Locate every blood parasite and identify its species.
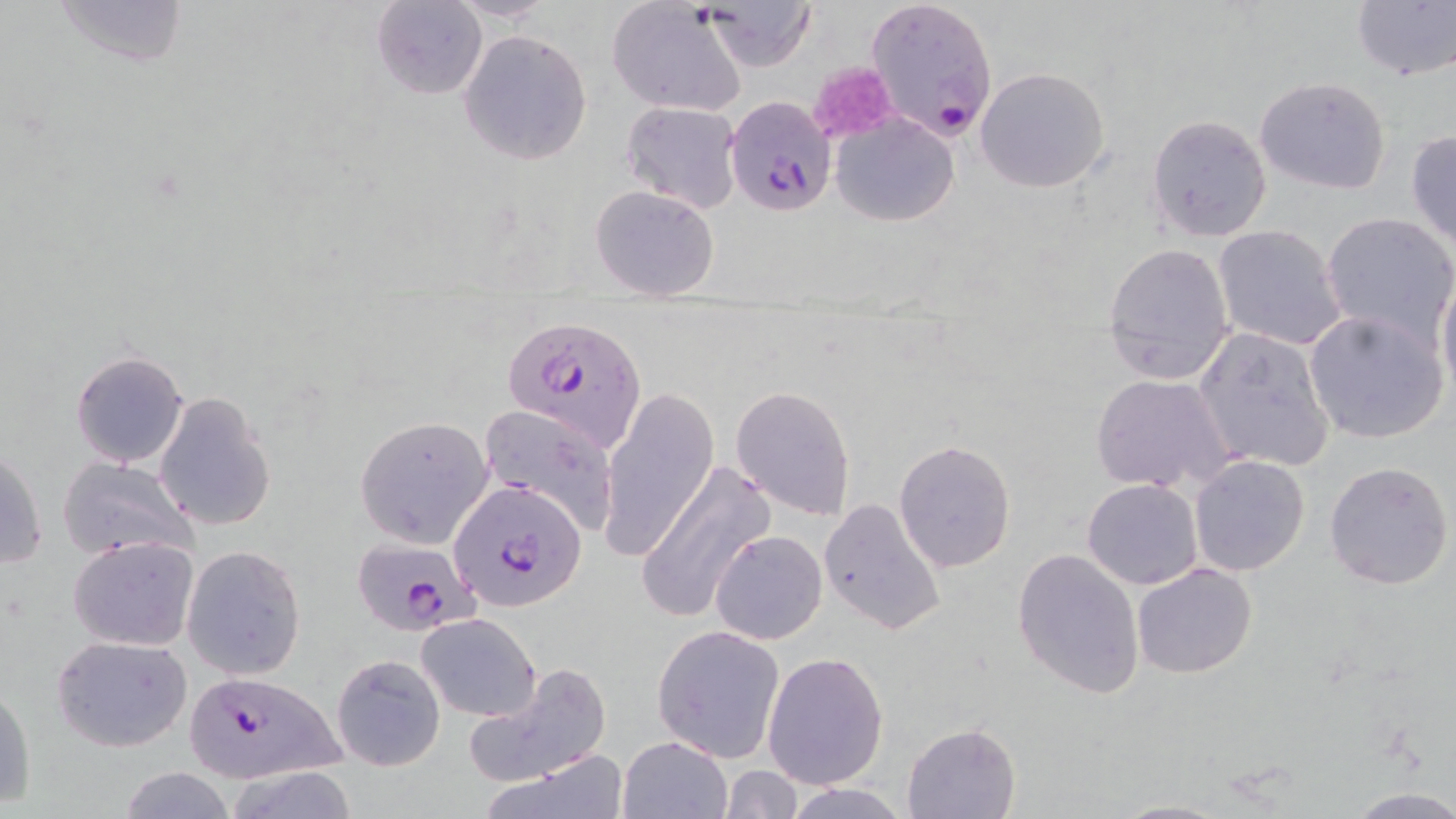
Approximate bounding boxes as (x1, y1, x2, y2) in pixels.
Plasmodium falciparum-infected red blood cells: (868, 0, 999, 141), (722, 94, 833, 216), (503, 313, 648, 454), (450, 478, 587, 610), (351, 536, 481, 635), (177, 670, 350, 782).
No Plasmodium ovale, Plasmodium malariae, Plasmodium vivax, Babesia divergens, or Trypanosoma brucei observed.

slide-level diagnosis = Plasmodium falciparum
field of view = single
platelet locations = approximate bounding boxes as (x1, y1, x2, y2) in pixels: (809, 61, 895, 144)
stain = May-Grünwald-Giemsa
modality = light microscopy
image size = 1456×819 pixels
magnification = 1000x
preparation = thin blood smear
uninfected red blood cell locations = approximate bounding boxes as (x1, y1, x2, y2) in pixels: (50, 0, 190, 69), (446, 0, 557, 24), (1351, 0, 1456, 81), (372, 1, 486, 102), (705, 1, 816, 71), (609, 3, 748, 118), (458, 29, 591, 165), (976, 67, 1110, 193), (1254, 76, 1391, 193), (621, 101, 743, 213), (831, 112, 959, 227), (1146, 114, 1272, 242), (1404, 129, 1456, 247), (589, 183, 721, 299), (1320, 213, 1456, 347), (1212, 224, 1351, 352), (1102, 242, 1236, 385), (1437, 273, 1456, 404), (1302, 308, 1449, 445), (1196, 327, 1335, 473), (70, 350, 190, 469), (1091, 373, 1240, 495), (730, 385, 857, 521), (600, 386, 720, 561), (153, 392, 277, 532), (480, 403, 622, 535), (354, 416, 494, 547), (893, 440, 1016, 571), (1, 446, 48, 572), (1189, 454, 1310, 575), (58, 456, 197, 559), (1323, 460, 1454, 591), (638, 463, 773, 624), (1082, 478, 1203, 589), (818, 498, 947, 636), (711, 527, 827, 645), (68, 536, 198, 650), (182, 544, 308, 681), (1011, 547, 1145, 698), (1132, 561, 1258, 678), (417, 614, 540, 722), (651, 624, 786, 761), (52, 636, 192, 752), (763, 651, 890, 791), (332, 654, 445, 771), (462, 662, 612, 786), (1, 682, 36, 810), (901, 722, 1019, 819), (618, 735, 730, 818), (484, 751, 627, 819), (721, 765, 801, 819), (117, 766, 238, 819), (223, 766, 361, 819), (782, 783, 910, 818), (1344, 787, 1456, 818), (1108, 798, 1236, 819)